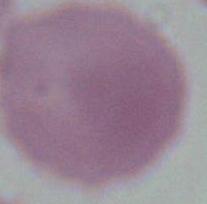

modality = photomicrograph
identification = erythrocyte
magnification = 1000x